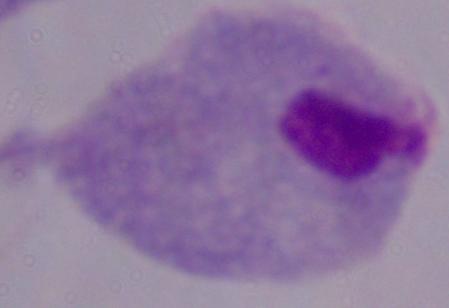
Summary:
  - Modality: micrograph
  - Identification: trichomonad
  - Magnification: 1000x